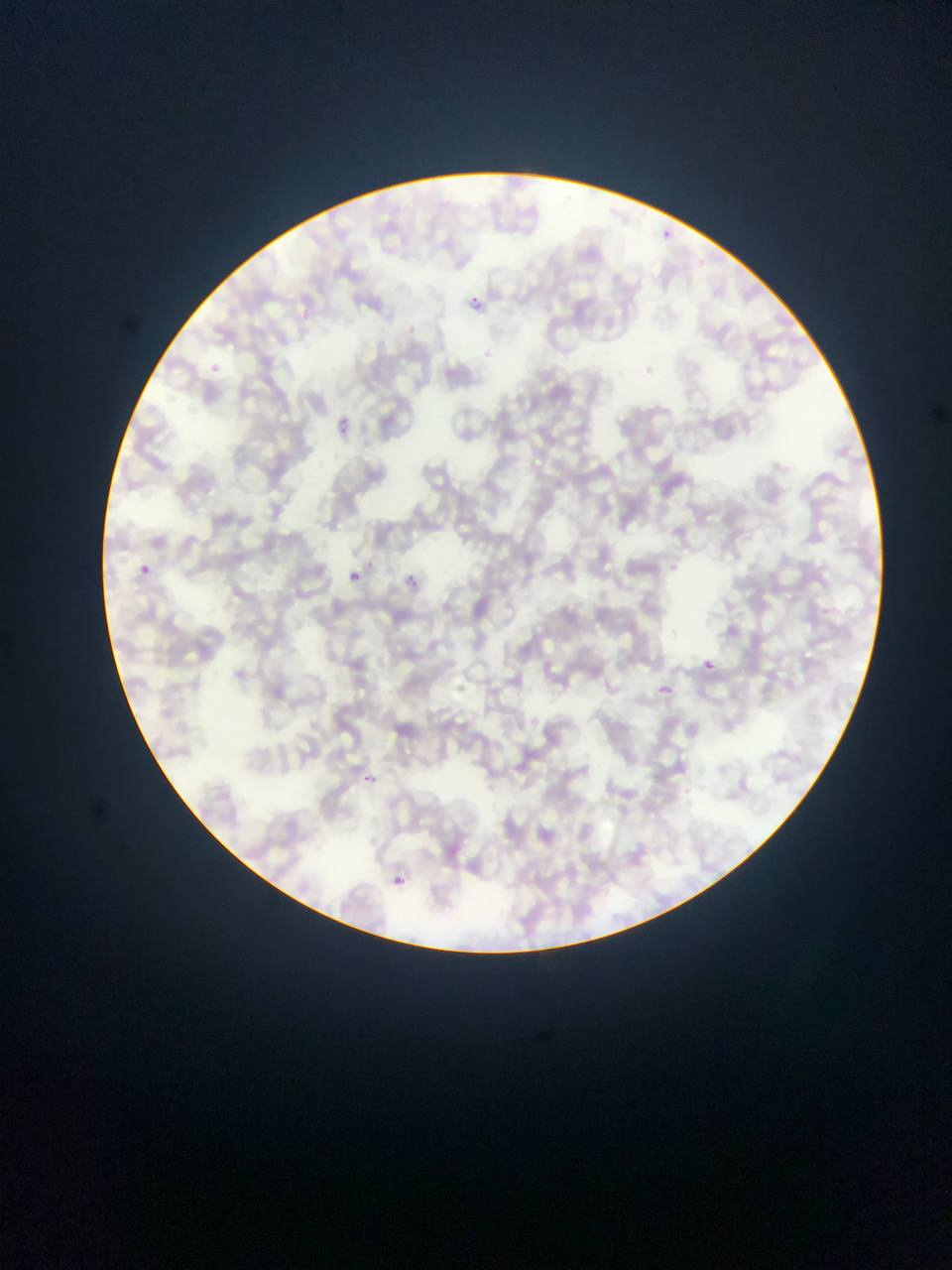 Approximate bounding boxes as left top right bottom in pixels. Malaria parasite locations: 657 228 678 240; 470 295 492 311; 332 409 352 424; 332 423 351 440; 141 557 153 574; 140 564 151 575; 349 570 360 582; 402 574 418 588; 702 660 714 672; 654 682 676 691; 359 774 379 788; 391 874 414 884. Sample from Ghana. Photographed through a microscope with a mobile-phone camera. Image is 952×1270 pixels. Single field of view. Thin blood smear.